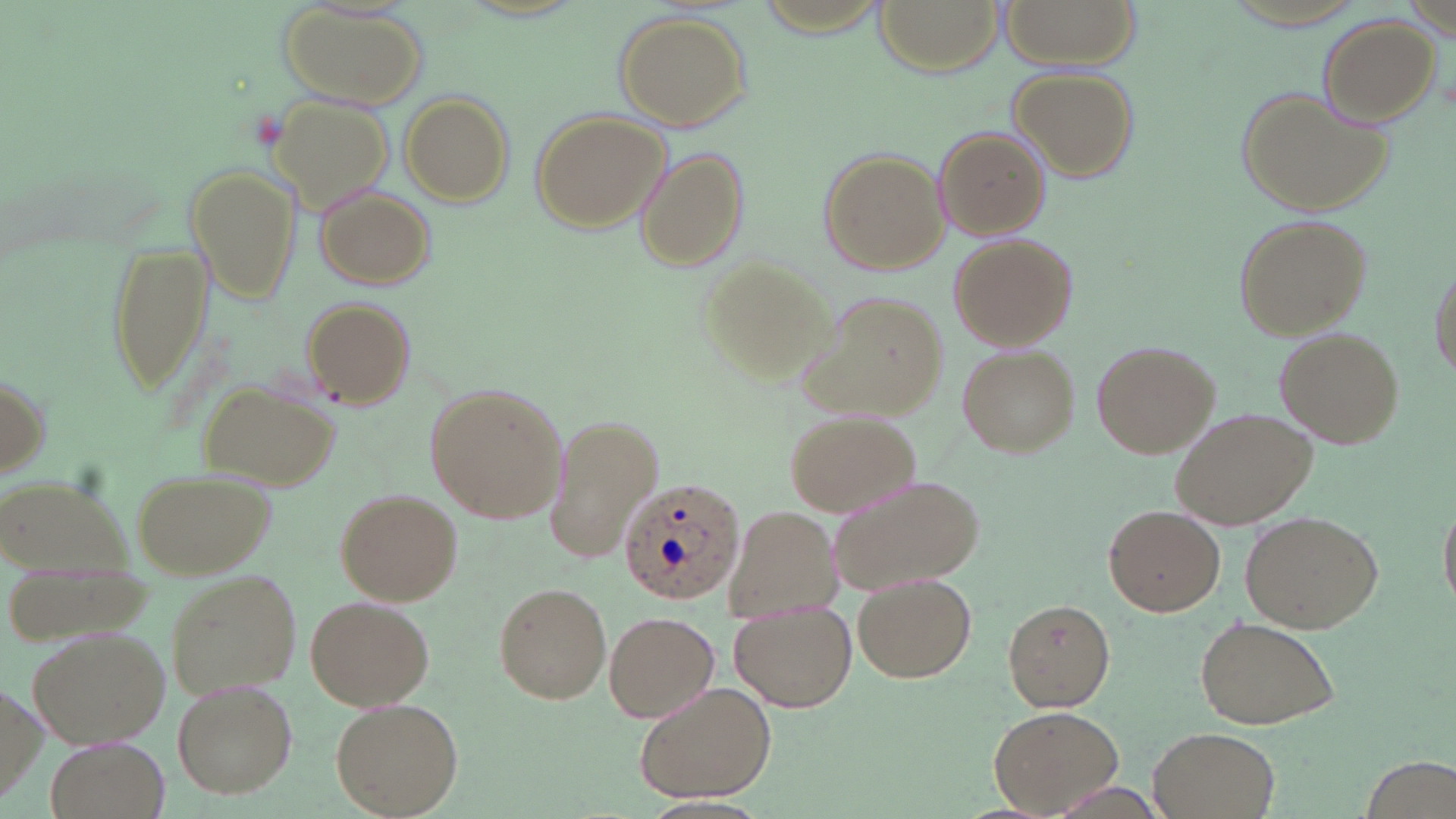 Approximate bounding boxes as [x1, y1, x2, y2] in pixels. Plasmodium ovale-infected red blood cell locations: [616, 476, 745, 607]. Uninfected red blood cell locations: [873, 0, 1002, 74], [1004, 0, 1136, 66], [280, 5, 426, 109], [614, 12, 753, 130], [1315, 15, 1442, 126], [1006, 65, 1139, 183], [1237, 86, 1396, 217], [400, 92, 515, 207], [273, 96, 392, 209], [529, 109, 669, 235], [934, 126, 1050, 241], [817, 146, 949, 276], [637, 149, 747, 271], [184, 166, 300, 305], [313, 185, 436, 291], [1231, 212, 1374, 341], [946, 233, 1076, 352], [105, 236, 217, 396], [696, 254, 833, 384], [1430, 261, 1455, 386], [802, 289, 948, 420], [299, 296, 416, 408], [1274, 327, 1404, 448], [1092, 340, 1218, 458], [958, 345, 1079, 457], [1, 370, 51, 481], [198, 377, 338, 491], [425, 383, 566, 525], [1171, 407, 1317, 532], [785, 411, 920, 516], [546, 416, 664, 567], [132, 471, 273, 580], [826, 472, 986, 594], [0, 475, 128, 577], [337, 489, 461, 605], [1437, 497, 1455, 615], [727, 505, 844, 625], [1104, 505, 1224, 616], [1239, 510, 1384, 633], [164, 568, 301, 697], [853, 572, 980, 683], [493, 582, 613, 705], [307, 596, 434, 712], [1002, 598, 1116, 713], [730, 605, 856, 713], [604, 611, 720, 722], [1193, 614, 1341, 731], [28, 624, 172, 749], [172, 678, 298, 799], [636, 682, 776, 805], [330, 698, 462, 818], [988, 704, 1122, 818], [1149, 727, 1278, 819], [42, 735, 172, 819]. Slide-level diagnosis: Plasmodium ovale. Optical microscopy. Thin blood smear. Image is 1456×819 pixels. Captured at 1000x magnification. May-Grünwald-Giemsa stain. Single field of view.